Comment on the morphology of the erythrocytes.
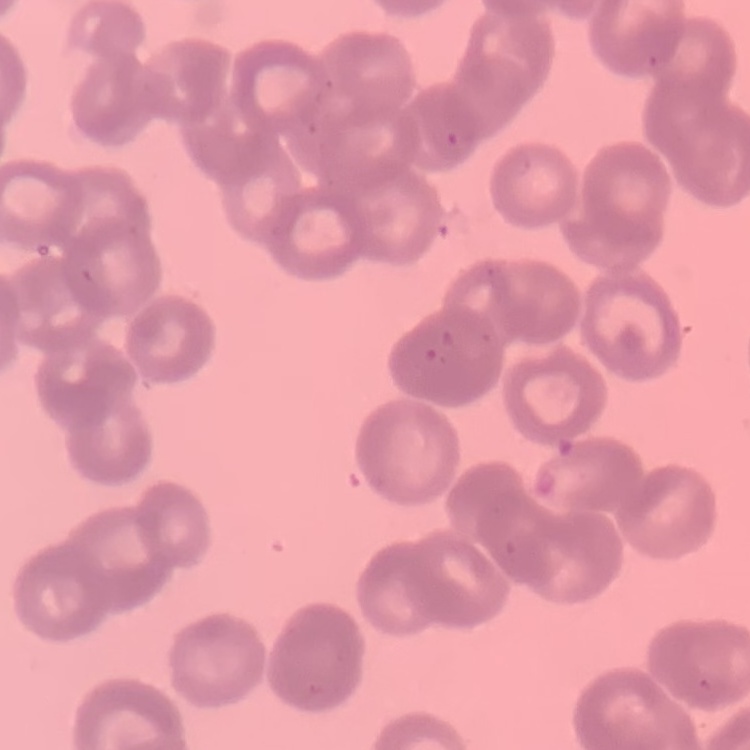

They show rouleaux formation.

Summary:
  - Stain: Field's or Giemsa
  - Preparation: thin peripheral smear
  - Image type: square crop of a larger photomicrograph